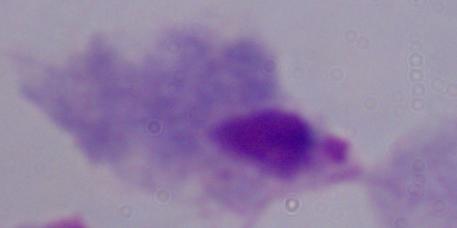 1000x magnification. Micrograph. A trichomonad is seen.